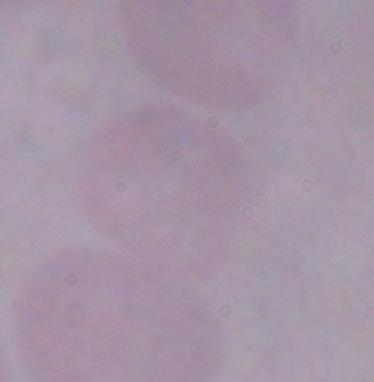
Summary:
  - Identification: trypanosome
  - Modality: photomicrograph
  - Magnification: 1000x